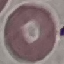

Result: no malaria parasites detected. Giemsa stain. Photographed with a smartphone camera at the microscope eyepiece. Thin blood smear. Automatically extracted cell patch, resized to 64 × 64 pixels.